Identify the parasite.
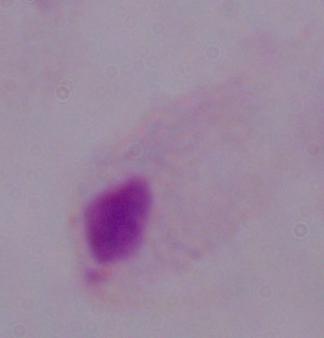

This is a trichomonad.

modality: photomicrograph
magnification: 1000x